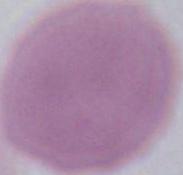
A red blood cell is shown. Captured at 1000x magnification. Photomicrograph.